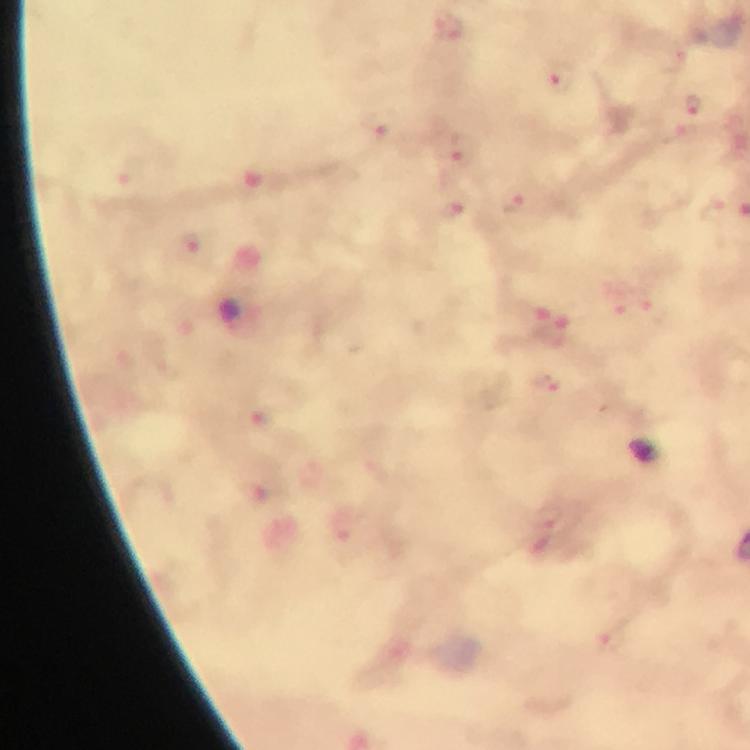

Approximate centers as {x, y} in pixels.
Summary:
  - Malaria parasite locations: {563, 83}, {694, 106}, {462, 151}, {514, 201}, {454, 214}, {548, 386}
  - Stain: Giemsa
  - Capture: smartphone photograph through a microscope
  - Magnification: 100x
  - Image size: 750×750 pixels
  - Immersion oil: applied
  - Context: from a malaria diagnostic workup
  - Preparation: thick blood smear
  - Cropped from: one field of view